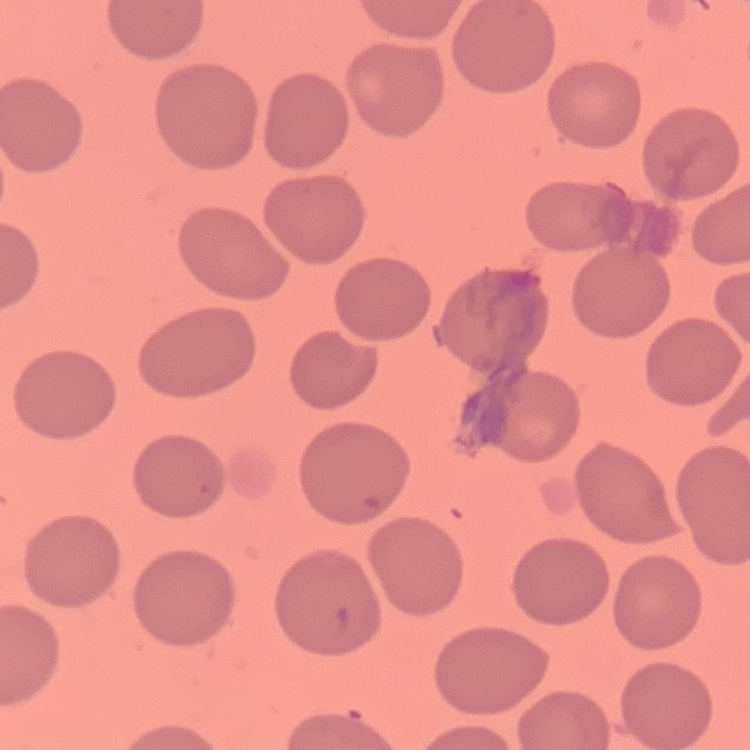

Summary:
  - Erythrocyte morphology: no rouleaux formation
  - Preparation: thin peripheral smear
  - Stain: Field's or Giemsa
  - Image type: square crop of a larger photomicrograph